Outline each blood parasite and name the species.
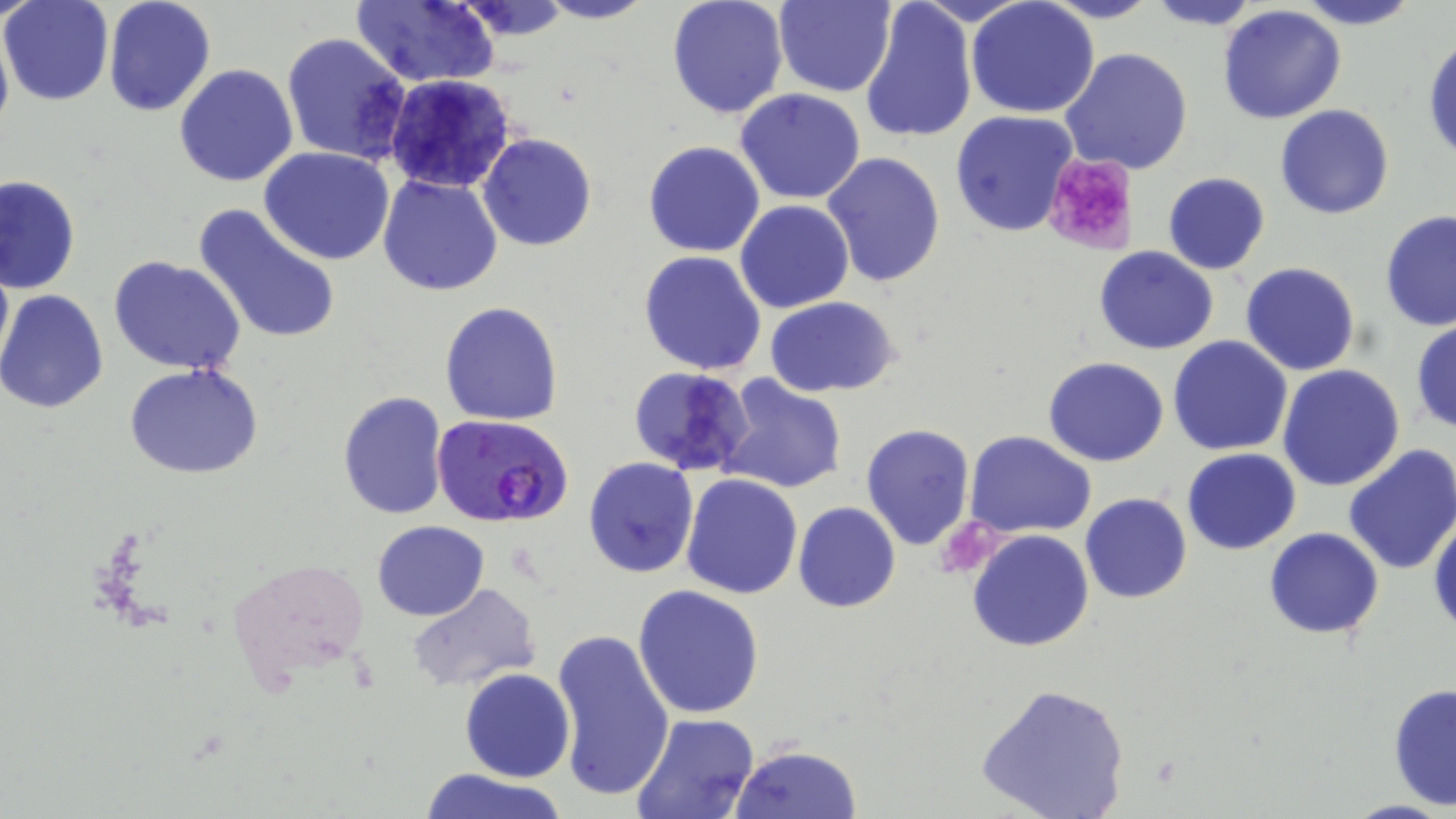
Approximate bounding boxes as named x1/y1/x2/y2 corners in pixels.
Plasmodium falciparum-infected red blood cells: (x1=430, y1=412, x2=576, y2=529).
No Plasmodium ovale, Plasmodium malariae, Plasmodium vivax, Babesia divergens, or Trypanosoma brucei observed.

slide-level diagnosis = Plasmodium falciparum
field of view = single
modality = optical microscopy
preparation = thin blood smear
magnification = 1000x
platelet locations = approximate bounding boxes as named x1/y1/x2/y2 corners in pixels: (x1=1043, y1=153, x2=1136, y2=256)
image size = 1456×819 pixels
stain = May-Grünwald-Giemsa
uninfected red blood cell locations = approximate bounding boxes as named x1/y1/x2/y2 corners in pixels: (x1=2, y1=0, x2=114, y2=105), (x1=102, y1=0, x2=215, y2=117), (x1=352, y1=0, x2=503, y2=88), (x1=454, y1=0, x2=572, y2=39), (x1=536, y1=0, x2=653, y2=24), (x1=665, y1=0, x2=789, y2=120), (x1=1041, y1=0, x2=1159, y2=24), (x1=1146, y1=0, x2=1260, y2=31), (x1=1293, y1=0, x2=1423, y2=30), (x1=772, y1=1, x2=896, y2=97), (x1=967, y1=1, x2=1098, y2=118), (x1=859, y1=2, x2=978, y2=145), (x1=1217, y1=6, x2=1347, y2=124), (x1=0, y1=21, x2=13, y2=144), (x1=281, y1=31, x2=413, y2=167), (x1=1424, y1=33, x2=1456, y2=164), (x1=1060, y1=48, x2=1193, y2=176), (x1=174, y1=63, x2=300, y2=187), (x1=381, y1=73, x2=519, y2=195), (x1=735, y1=88, x2=867, y2=205), (x1=1274, y1=104, x2=1395, y2=219), (x1=950, y1=110, x2=1081, y2=238), (x1=479, y1=134, x2=597, y2=253), (x1=643, y1=140, x2=765, y2=257), (x1=260, y1=147, x2=395, y2=265), (x1=821, y1=150, x2=947, y2=289), (x1=377, y1=173, x2=504, y2=296), (x1=1162, y1=173, x2=1270, y2=274), (x1=0, y1=175, x2=80, y2=294), (x1=735, y1=199, x2=853, y2=312), (x1=191, y1=203, x2=342, y2=346), (x1=683, y1=209, x2=808, y2=346), (x1=1380, y1=210, x2=1456, y2=334), (x1=1094, y1=248, x2=1218, y2=354), (x1=0, y1=250, x2=12, y2=384), (x1=639, y1=251, x2=767, y2=375), (x1=109, y1=255, x2=247, y2=374), (x1=1240, y1=261, x2=1361, y2=377), (x1=0, y1=289, x2=109, y2=415), (x1=765, y1=296, x2=902, y2=398), (x1=440, y1=301, x2=563, y2=425), (x1=1410, y1=318, x2=1456, y2=436), (x1=1168, y1=337, x2=1294, y2=456), (x1=1043, y1=357, x2=1169, y2=467), (x1=625, y1=363, x2=756, y2=479), (x1=125, y1=364, x2=263, y2=480), (x1=1277, y1=365, x2=1405, y2=492), (x1=715, y1=374, x2=848, y2=495), (x1=337, y1=391, x2=450, y2=520), (x1=860, y1=424, x2=976, y2=550), (x1=965, y1=432, x2=1096, y2=538), (x1=1343, y1=443, x2=1456, y2=576), (x1=1183, y1=448, x2=1300, y2=553), (x1=583, y1=456, x2=699, y2=578), (x1=680, y1=474, x2=803, y2=598), (x1=1080, y1=492, x2=1192, y2=603), (x1=793, y1=502, x2=901, y2=615), (x1=1429, y1=513, x2=1456, y2=634), (x1=371, y1=520, x2=489, y2=620), (x1=1264, y1=527, x2=1384, y2=638), (x1=966, y1=528, x2=1095, y2=652), (x1=225, y1=552, x2=373, y2=702), (x1=407, y1=583, x2=542, y2=695), (x1=632, y1=585, x2=765, y2=720), (x1=550, y1=627, x2=675, y2=802), (x1=460, y1=668, x2=575, y2=782), (x1=1388, y1=681, x2=1456, y2=814), (x1=974, y1=682, x2=1130, y2=819), (x1=631, y1=713, x2=761, y2=819), (x1=729, y1=744, x2=863, y2=819), (x1=418, y1=767, x2=569, y2=819)